Assess this cell for malaria.
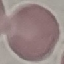

Uninfected.

Summary:
  - Stain: Giemsa
  - Image type: automatically extracted cell patch, resized to 64 × 64 pixels
  - Capture: smartphone camera at the microscope eyepiece
  - Preparation: thin blood film